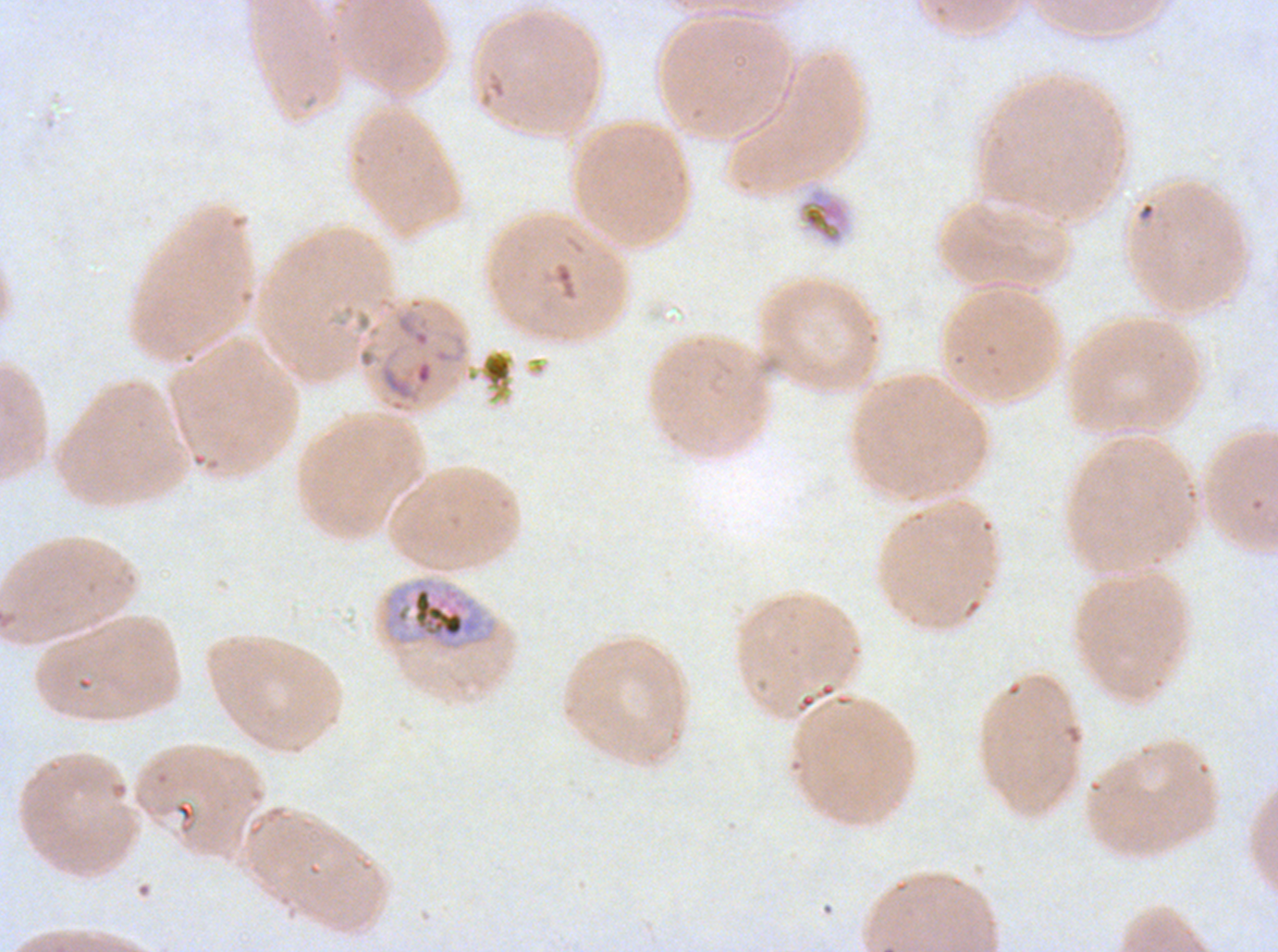

Approximate bounding rectangles given as corner coordinates in pixels from the top-left.
Summary:
  - Debris locations: (x1=796, y1=187, x2=850, y2=245)
  - Early schizont locations: (x1=381, y1=577, x2=497, y2=652)
  - Image size: 1278×952 pixels
  - Specimen: ex-vivo P. falciparum culture from a patient in The Gambia, grown for 24 to 48 hours
  - Field of view: one sub-image of a larger composite
  - Stain: Giemsa
  - Preparation: thin blood smear